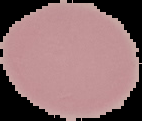

Summary:
  - Image type: cell region segmented out of the field of view; surrounding area masked to black
  - Result: no Plasmodium parasites detected
  - Preparation: thin blood smear
  - Image size: 142×121 pixels